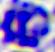
Summary:
  - Identification: leukocyte
  - Modality: photomicrograph
  - Magnification: 400x